Give the position of every leukocyte visible.
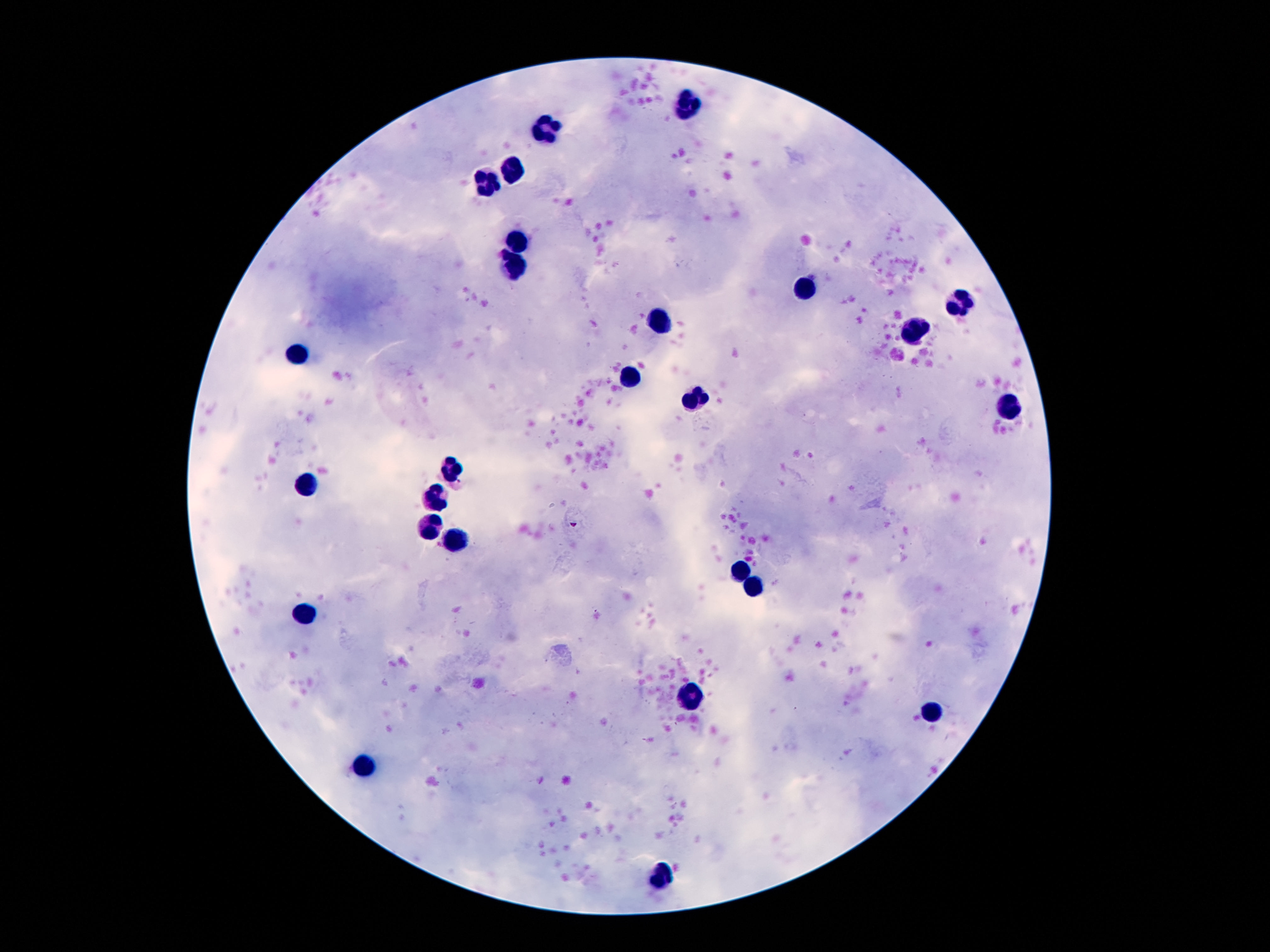
Approximate centers as [x, y] in pixels.
Leukocytes: [689, 108], [548, 131], [516, 168], [488, 175], [516, 239], [514, 266], [810, 288], [959, 301], [662, 319], [916, 329], [304, 352], [631, 379], [695, 398], [1009, 408], [452, 471], [309, 487], [439, 498], [432, 526], [455, 540], [738, 571], [757, 587], [306, 613], [693, 700], [928, 712], [366, 765], [664, 873].

100x magnification. One field from this slide. Photographed through the microscope eyepiece with a smartphone camera. Image is 1270×952 pixels. Giemsa-stained preparation. Patient malaria status: not infected. Thick blood film.